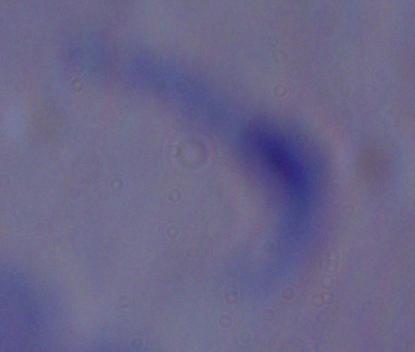

Micrograph. A trypanosome is shown. Captured at 1000x magnification.